Name the parasite shown.
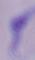
This is a trypanosome.

Micrograph. 1000x magnification.